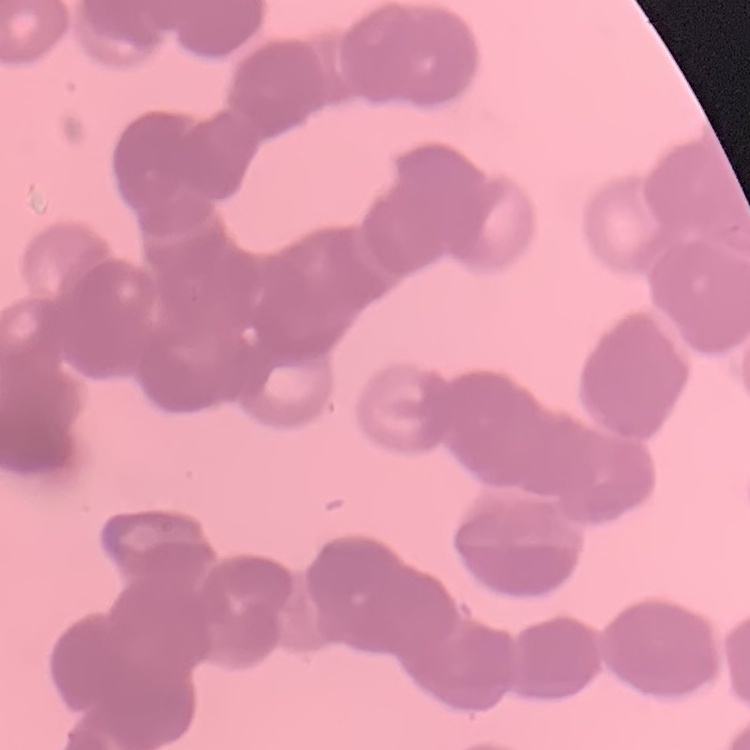

red_blood_cell_morphology: rouleaux formation
stain: Field's or Giemsa
preparation: thin blood film
image_type: square crop of a larger photomicrograph